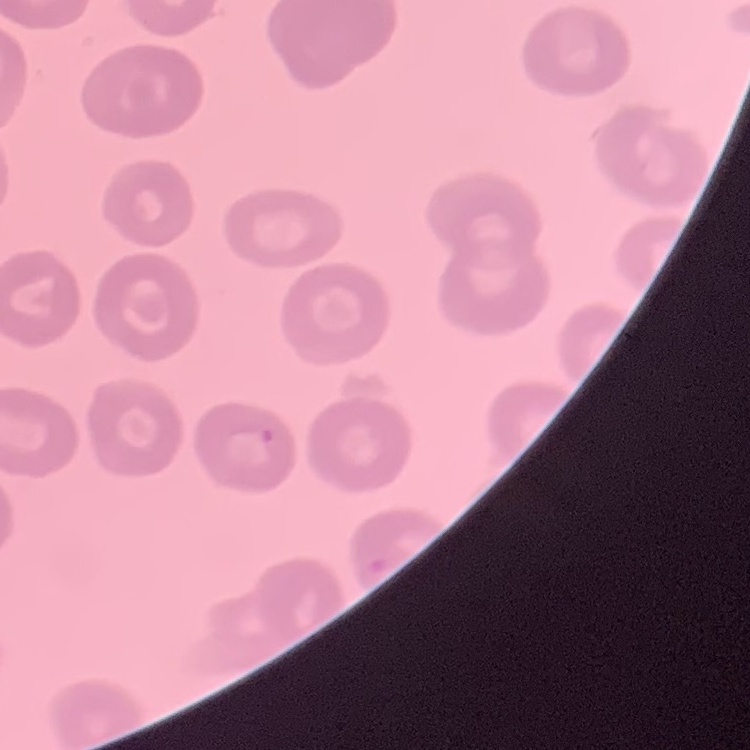

Summary:
  - Erythrocyte morphology: no rouleaux formation
  - Preparation: thin peripheral smear
  - Stain: Field's or Giemsa
  - Image type: one tile cut from a larger photomicrograph